Describe the morphology of the red blood cells.
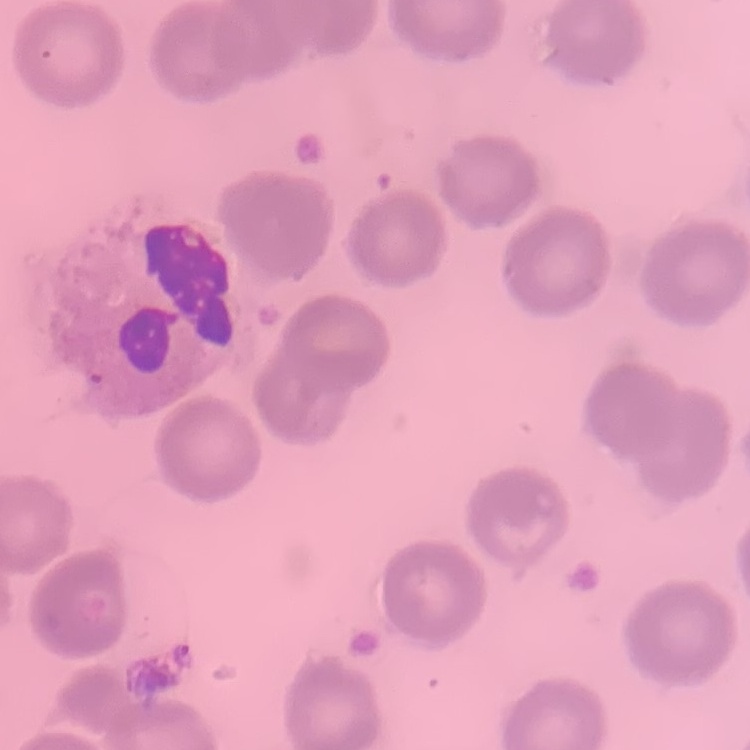
They show no rouleaux formation.

{
  "image_type": "one tile cut from a larger photomicrograph",
  "preparation": "thin blood smear",
  "stain": "Field's or Giemsa"
}